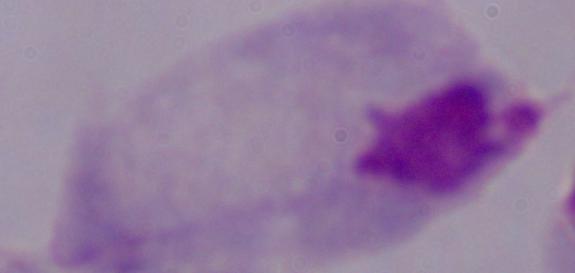
Summary:
  - Identification: trichomonad
  - Modality: micrograph
  - Magnification: 1000x